Assess this cell for malaria.
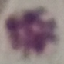
It is uninfected.

Summary:
  - Capture: smartphone through the microscope eyepiece
  - Preparation: thin blood smear
  - Image type: cell patch, automatically extracted from a larger field of view and resized to 64 × 64 pixels
  - Stain: Giemsa